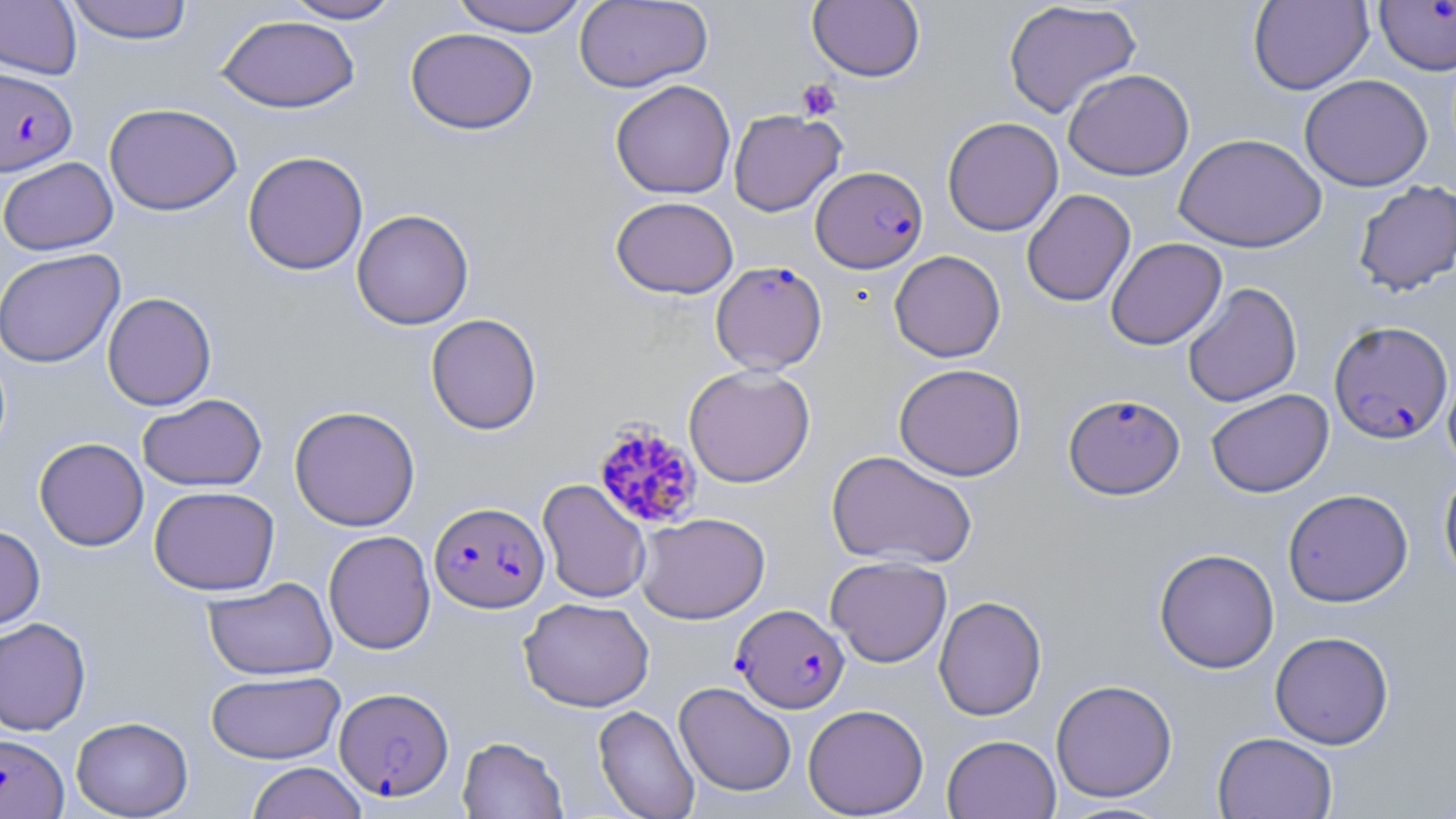

plasmodium_falciparum_infected_red_blood_cell_locations: 'approximate bounding boxes as (x1,y1)-(x2,y2) corner pairs in pixels: (1374,0)-(1456,75), (1,67)-(77,176), (810,165)-(927,273), (710,260)-(827,375), (1329,320)-(1453,444), (1063,393)-(1185,499), (594,421)-(704,530), (429,501)-(550,613), (732,604)-(849,713), (337,699)-(456,800), (0,733)-(68,818)'
slide_level_diagnosis: Plasmodium falciparum
modality: optical microscopy
stain: May-Grünwald-Giemsa
uninfected_red_blood_cell_locations: 'approximate bounding boxes as (x1,y1)-(x2,y2) corner pairs in pixels: (65,0)-(194,44), (282,0)-(404,24), (450,0)-(588,36), (574,0)-(713,93), (1248,0)-(1373,95), (0,1)-(82,79), (808,1)-(925,82), (1003,1)-(1142,119), (216,14)-(360,113), (405,27)-(537,134), (1062,68)-(1194,181), (1299,74)-(1432,191), (610,79)-(736,199), (104,102)-(242,216), (728,109)-(846,216), (942,116)-(1063,236), (1174,133)-(1326,252), (242,151)-(368,275), (0,157)-(118,255), (1352,179)-(1456,296), (1021,189)-(1136,307), (610,196)-(739,299), (351,209)-(474,330), (1105,237)-(1227,350), (0,249)-(125,368), (889,250)-(1005,362), (1182,282)-(1303,407), (102,292)-(217,411), (425,313)-(542,435), (1443,362)-(1456,475), (894,363)-(1026,481), (684,364)-(815,488), (1205,388)-(1334,498), (137,393)-(267,492), (289,405)-(420,531), (34,437)-(149,551), (826,450)-(978,570), (1439,470)-(1456,588), (537,479)-(651,604), (149,486)-(280,596), (1283,488)-(1413,607), (635,512)-(770,624), (0,524)-(45,632), (323,530)-(436,654), (1153,548)-(1279,674), (825,555)-(952,667), (203,577)-(337,681), (933,595)-(1047,721), (518,596)-(655,712), (0,617)-(91,736), (1269,631)-(1394,749), (206,670)-(344,764), (1051,679)-(1178,803), (674,681)-(797,796), (803,703)-(929,818), (593,705)-(699,819), (71,716)-(193,818), (1213,731)-(1338,819), (942,734)-(1061,819), (457,736)-(568,818), (246,762)-(367,819)'
preparation: thin blood film
magnification: 1000x
image_size: 1456×819 pixels
platelet_locations: 'approximate bounding boxes as (x1,y1)-(x2,y2) corner pairs in pixels: (796,79)-(842,121)'
field_of_view: one of a larger specimen